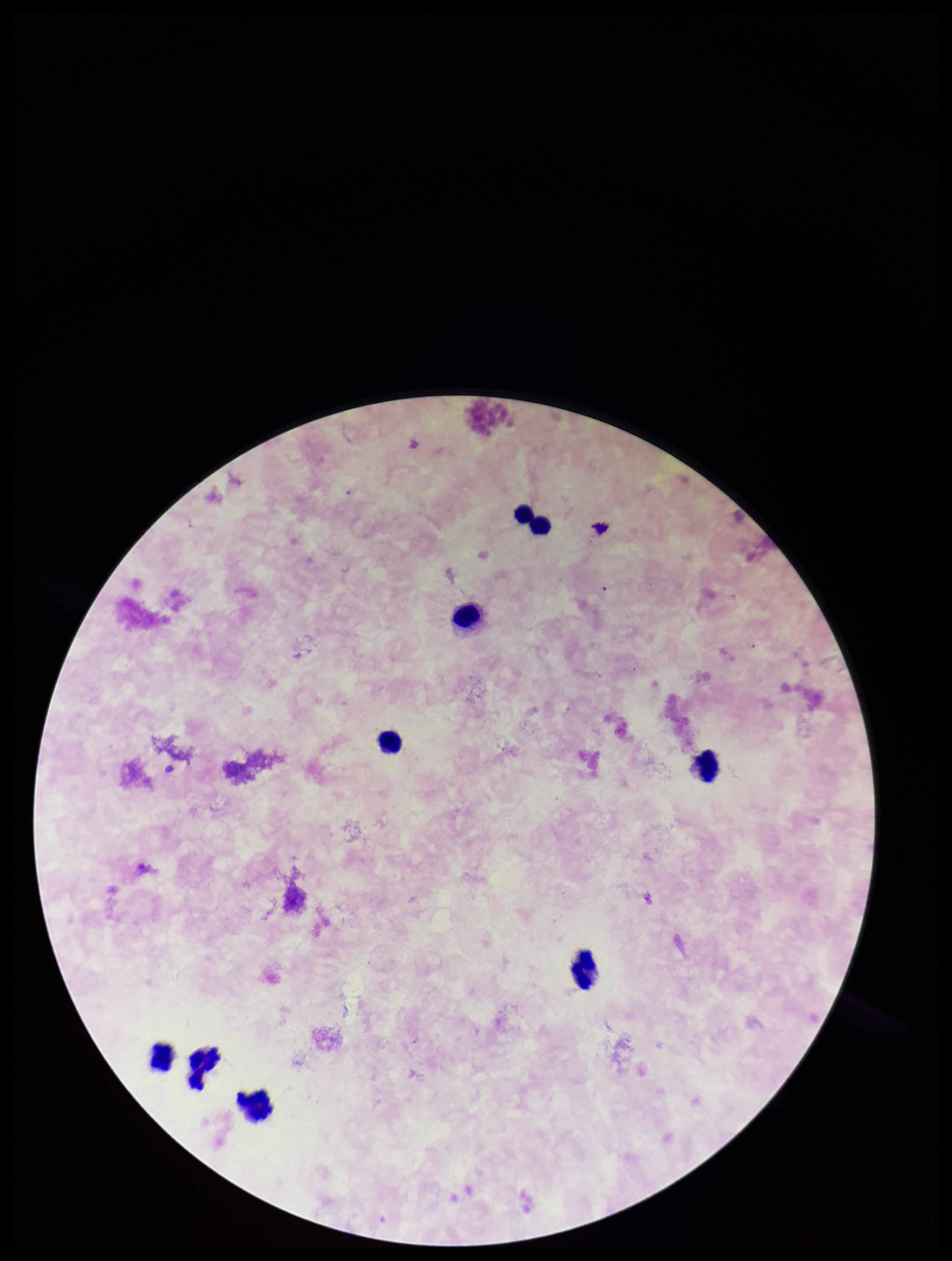

Parasite count: 0. Giemsa stain. Leukocyte count: 9. Smartphone photograph taken through the eyepiece of a microscope. Plasmodium parasites: none identified. One field from this slide. Image is 952×1261 pixels. Preparation: thick blood smear. Patient malaria status: negative.